Assess this cell for malaria.
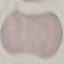
Uninfected.

Summary:
  - Stain: Giemsa
  - Preparation: thin blood smear
  - Capture: smartphone through the microscope eyepiece
  - Image type: cell patch, automatically extracted from a larger field of view and resized to 64 × 64 pixels